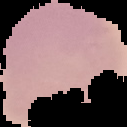

Summary:
  - Result: no malaria parasites seen
  - Image size: 127×127 pixels
  - Image type: cell region segmented out of the field of view; surrounding area masked to black
  - Preparation: thin blood film